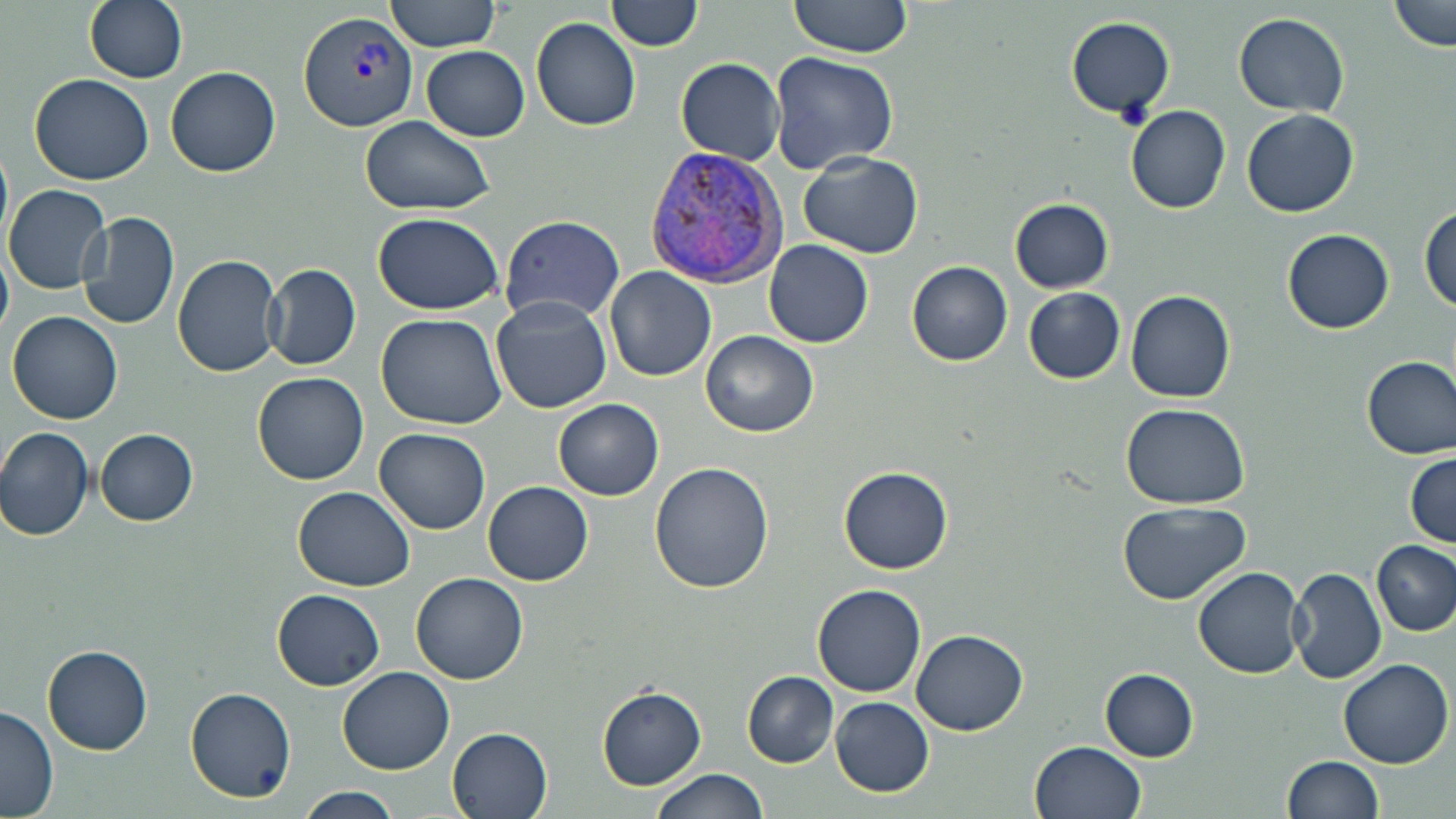 Approximate bounding boxes as (x1,y1)-(x2,y2) corner pairs in pixels. Uninfected red blood cell locations: (84,0)-(187,83), (386,0)-(504,54), (785,0)-(914,57), (1387,0)-(1454,53), (606,1)-(703,51), (1234,12)-(1350,117), (1065,15)-(1176,119), (531,17)-(642,131), (422,46)-(530,141), (767,50)-(899,175), (676,58)-(786,164), (165,65)-(281,177), (30,72)-(155,185), (1125,104)-(1231,213), (1242,109)-(1359,218), (361,114)-(496,216), (798,149)-(924,259), (4,182)-(112,295), (1009,197)-(1115,293), (1420,207)-(1455,313), (77,210)-(179,330), (373,212)-(505,314), (498,216)-(626,323), (1283,228)-(1394,333), (764,239)-(874,348), (0,248)-(12,338), (172,252)-(284,378), (906,260)-(1011,365), (265,262)-(360,370), (605,267)-(717,382), (1024,288)-(1126,385), (1125,289)-(1236,403), (491,295)-(614,415), (8,310)-(124,425), (375,312)-(509,429), (701,329)-(818,437), (1361,354)-(1456,460), (252,372)-(368,485), (554,398)-(663,500), (1122,402)-(1251,507), (0,427)-(95,542), (374,428)-(492,534), (95,429)-(199,526), (1405,451)-(1455,547), (650,461)-(777,592), (840,467)-(953,574), (483,480)-(593,585), (294,487)-(418,592), (1118,502)-(1250,605), (1373,541)-(1455,635), (1192,566)-(1305,678), (1286,566)-(1387,684), (412,572)-(527,684), (812,584)-(927,698), (271,588)-(385,691), (912,628)-(1030,734), (43,646)-(152,757), (1337,657)-(1453,767), (338,666)-(454,775), (1100,668)-(1198,762), (743,672)-(839,767), (597,685)-(708,790), (186,687)-(296,804), (830,697)-(933,795), (0,705)-(59,818), (446,726)-(554,819), (1030,741)-(1147,819), (1284,755)-(1385,819), (651,769)-(766,819), (297,787)-(406,818). Plasmodium vivax-infected red blood cell locations: (298,12)-(418,132), (648,146)-(790,287). Slide-level diagnosis: Plasmodium vivax. Image is 1456×819 pixels. Single field of view. Optical microscopy. May-Grünwald-Giemsa stain. 1000x magnification. Thin blood smear.